Assess this cell for malaria.
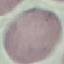

It is uninfected.

Photographed with a smartphone camera at the microscope eyepiece. Thin smear of blood. Giemsa-stained preparation. Automatically extracted cell patch, resized to 64 × 64 pixels.